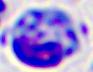

Summary:
  - Modality: micrograph
  - Magnification: 400x
  - Identification: white blood cell